Identify the parasite.
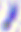
Toxoplasma gondii.

Photomicrograph. Captured at 400x magnification.